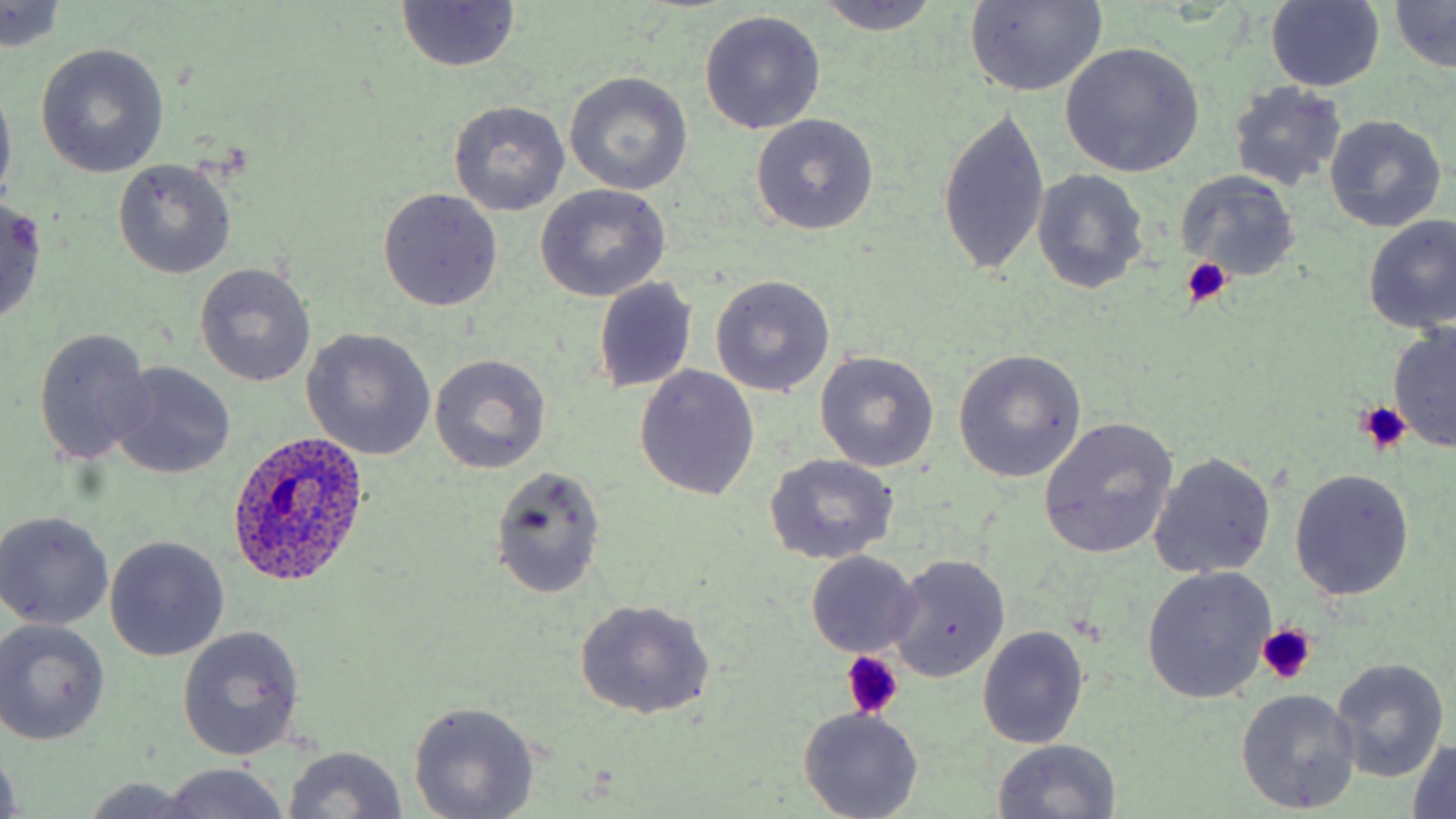
Summary:
  - Coordinate format: approximate bounding boxes as named x1/y1/x2/y2 corners in pixels
  - Platelet locations: (x1=1177, y1=257, x2=1233, y2=306), (x1=1357, y1=403, x2=1411, y2=454), (x1=1255, y1=626, x2=1316, y2=688), (x1=840, y1=653, x2=903, y2=721)
  - Uninfected red blood cell locations: (x1=811, y1=0, x2=943, y2=36), (x1=1390, y1=0, x2=1456, y2=73), (x1=1265, y1=1, x2=1386, y2=90), (x1=396, y1=3, x2=523, y2=74), (x1=963, y1=3, x2=1107, y2=96), (x1=0, y1=4, x2=68, y2=53), (x1=699, y1=9, x2=826, y2=135), (x1=34, y1=42, x2=170, y2=178), (x1=1059, y1=42, x2=1205, y2=178), (x1=564, y1=71, x2=693, y2=194), (x1=0, y1=76, x2=17, y2=207), (x1=1227, y1=82, x2=1349, y2=191), (x1=450, y1=101, x2=569, y2=217), (x1=935, y1=104, x2=1051, y2=280), (x1=749, y1=114, x2=879, y2=235), (x1=1324, y1=115, x2=1446, y2=232), (x1=112, y1=158, x2=236, y2=279), (x1=1033, y1=170, x2=1149, y2=292), (x1=1179, y1=172, x2=1300, y2=281), (x1=535, y1=183, x2=671, y2=302), (x1=379, y1=188, x2=503, y2=312), (x1=554, y1=188, x2=689, y2=387), (x1=0, y1=197, x2=50, y2=327), (x1=1361, y1=215, x2=1456, y2=334), (x1=196, y1=262, x2=316, y2=386), (x1=710, y1=275, x2=837, y2=396), (x1=593, y1=278, x2=699, y2=393), (x1=1387, y1=322, x2=1456, y2=451), (x1=32, y1=327, x2=154, y2=465), (x1=301, y1=328, x2=436, y2=460), (x1=815, y1=350, x2=940, y2=472), (x1=953, y1=351, x2=1086, y2=484), (x1=429, y1=354, x2=552, y2=474), (x1=110, y1=362, x2=236, y2=479), (x1=635, y1=365, x2=760, y2=502), (x1=1038, y1=417, x2=1179, y2=560), (x1=764, y1=453, x2=899, y2=565), (x1=1148, y1=453, x2=1277, y2=579), (x1=488, y1=464, x2=606, y2=600), (x1=1289, y1=470, x2=1415, y2=600), (x1=0, y1=510, x2=115, y2=631), (x1=106, y1=536, x2=230, y2=662), (x1=805, y1=552, x2=922, y2=657), (x1=887, y1=554, x2=1010, y2=682), (x1=1142, y1=567, x2=1277, y2=705), (x1=573, y1=600, x2=716, y2=718), (x1=0, y1=620, x2=110, y2=745), (x1=178, y1=626, x2=305, y2=760), (x1=977, y1=626, x2=1090, y2=749), (x1=1330, y1=659, x2=1448, y2=783), (x1=1236, y1=688, x2=1361, y2=814), (x1=408, y1=701, x2=540, y2=818), (x1=798, y1=708, x2=924, y2=819), (x1=990, y1=739, x2=1124, y2=819), (x1=1408, y1=739, x2=1455, y2=819), (x1=283, y1=745, x2=409, y2=819), (x1=0, y1=746, x2=24, y2=819), (x1=160, y1=764, x2=290, y2=819), (x1=83, y1=778, x2=207, y2=818)
  - Plasmodium ovale-infected red blood cell locations: (x1=226, y1=433, x2=372, y2=588)
  - Slide-level diagnosis: Plasmodium ovale
  - Field of view: single
  - Magnification: 1000x
  - Modality: light microscopy
  - Preparation: thin blood smear
  - Stain: May-Grünwald-Giemsa
  - Image size: 1456×819 pixels